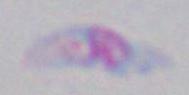 Micrograph. Toxoplasma gondii is shown. 1000x magnification.